Comment on the morphology of the erythrocytes.
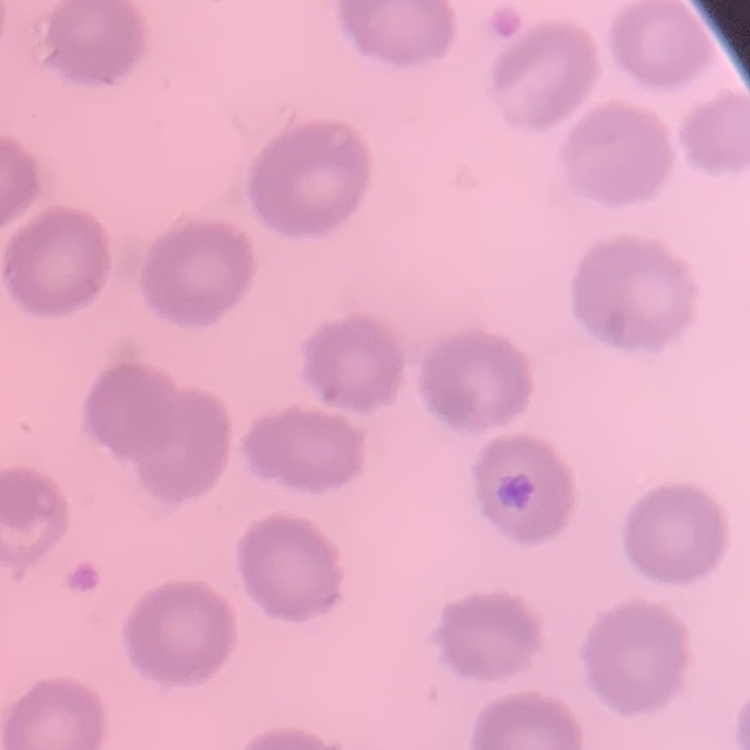

No rouleaux formation.

{
  "stain": "Field's or Giemsa",
  "preparation": "thin blood smear",
  "image_type": "one tile cut from a larger photomicrograph"
}